Comment on the morphology of the erythrocytes.
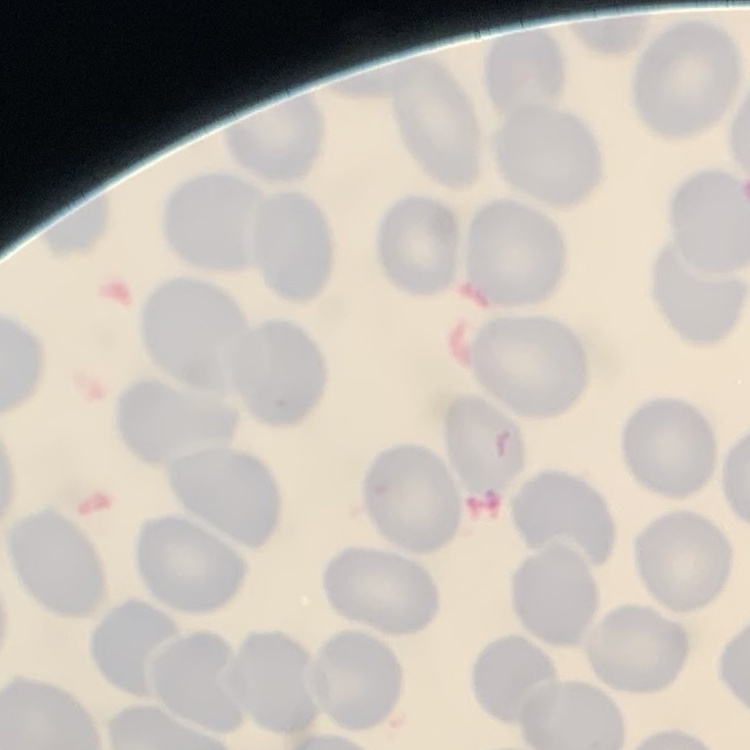

No rouleaux formation.

image_type: one tile cut from a larger photomicrograph
preparation: thin blood film
stain: Field's or Giemsa